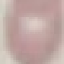
Summary:
  - Result: no malaria parasites detected
  - Stain: Giemsa
  - Capture: smartphone through the microscope eyepiece
  - Image type: cell patch, automatically extracted from a larger field of view and resized to 64 × 64 pixels
  - Preparation: thin blood smear